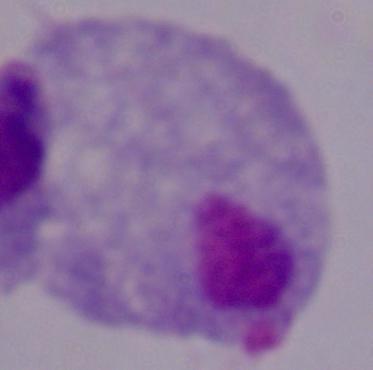

identification = trichomonad
modality = photomicrograph
magnification = 1000x